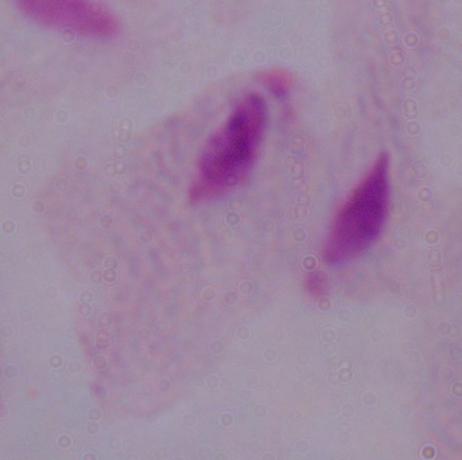
Summary:
  - Identification: trichomonad
  - Magnification: 1000x
  - Modality: micrograph